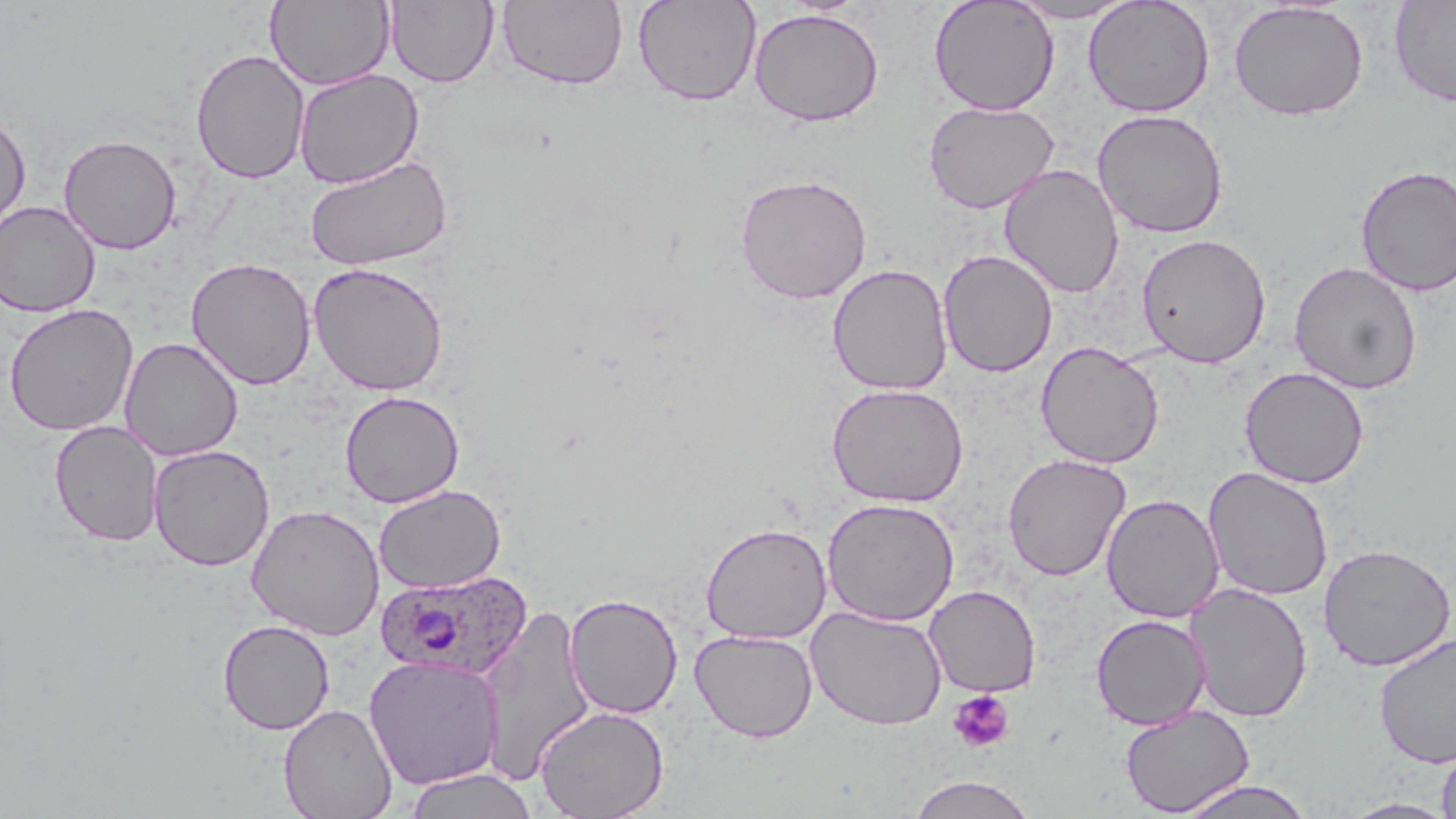
Summary:
  - Coordinate format: approximate bounding boxes as (x1, y1, x2, y2) in pixels
  - Uninfected red blood cell locations: (386, 0, 498, 87), (496, 0, 629, 91), (632, 0, 762, 106), (1004, 0, 1140, 23), (1083, 0, 1215, 118), (1389, 0, 1456, 107), (266, 1, 394, 91), (929, 1, 1059, 116), (1228, 1, 1369, 122), (749, 8, 884, 126), (190, 48, 310, 185), (293, 68, 424, 189), (923, 100, 1059, 213), (1092, 109, 1229, 238), (0, 112, 31, 236), (58, 134, 182, 254), (303, 155, 452, 270), (999, 163, 1124, 299), (1354, 164, 1456, 296), (735, 173, 872, 304), (0, 201, 100, 317), (1136, 232, 1271, 368), (937, 249, 1058, 377), (186, 257, 316, 390), (1288, 260, 1423, 395), (308, 261, 449, 397), (827, 263, 953, 395), (3, 303, 139, 436), (119, 336, 243, 462), (1036, 340, 1164, 469), (1239, 366, 1369, 489), (826, 382, 969, 507), (340, 390, 465, 508), (49, 420, 164, 546), (149, 444, 274, 571), (1003, 453, 1131, 581), (1203, 466, 1333, 602), (374, 484, 506, 594), (1101, 493, 1225, 623), (822, 498, 959, 627), (246, 503, 385, 640), (700, 522, 832, 645), (1318, 543, 1456, 671), (1185, 582, 1313, 723), (924, 584, 1041, 697), (564, 593, 683, 719), (478, 602, 595, 783), (806, 605, 947, 730), (1091, 614, 1211, 730), (217, 619, 335, 735), (690, 628, 818, 742), (1374, 632, 1456, 769), (364, 655, 505, 789), (278, 703, 398, 819), (534, 704, 668, 818), (1120, 705, 1254, 817), (1436, 742, 1456, 819), (403, 768, 537, 819), (907, 775, 1038, 819), (1174, 779, 1316, 819), (1340, 797, 1455, 818)
  - Platelet locations: (948, 689, 1014, 753)
  - Plasmodium ovale-infected red blood cell locations: (375, 569, 532, 679)
  - Slide-level diagnosis: Plasmodium ovale
  - Image size: 1456×819 pixels
  - Magnification: 1000x
  - Stain: May-Grünwald-Giemsa
  - Field of view: one of a larger specimen
  - Modality: light microscopy
  - Preparation: thin blood film